Locate every blood parasite and identify its species.
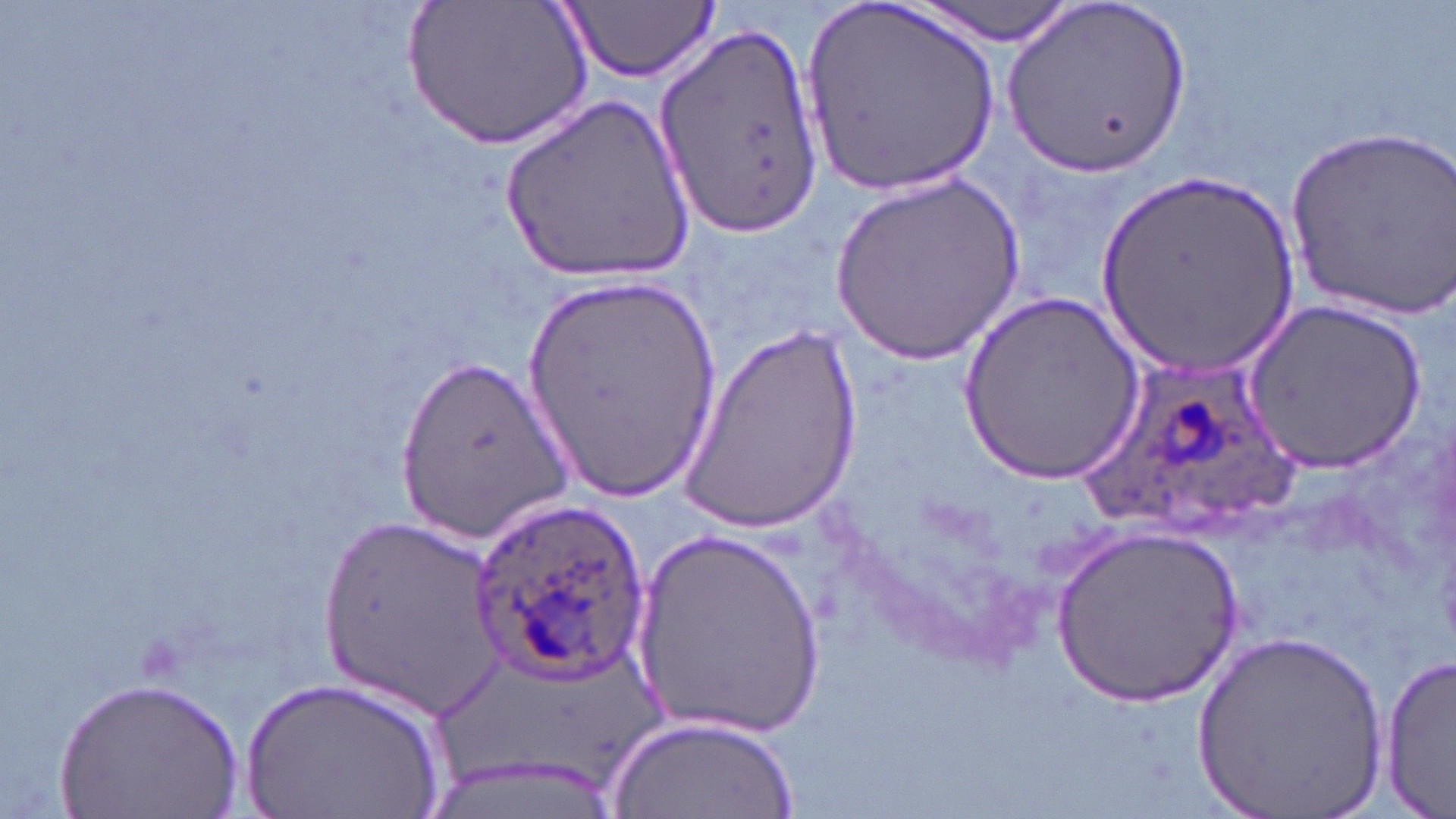

Approximate bounding boxes as [x1, y1, x2, y2] in pixels.
Plasmodium ovale-infected red blood cells: [1080, 354, 1309, 532], [468, 493, 653, 687].
No Plasmodium falciparum, Plasmodium malariae, Plasmodium vivax, Babesia divergens, or Trypanosoma brucei observed.

{
  "slide_level_diagnosis": "Plasmodium ovale",
  "magnification": "1000x",
  "preparation": "thin blood film",
  "image_size": "1456×819 pixels",
  "stain": "May-Grünwald-Giemsa",
  "modality": "light microscopy",
  "field_of_view": "one of a larger specimen",
  "uninfected_red_blood_cell_locations": "approximate bounding boxes as [x1, y1, x2, y2] in pixels: [407, 0, 591, 152], [560, 0, 720, 82], [907, 0, 1082, 43], [1005, 0, 1190, 177], [804, 3, 1000, 200], [658, 25, 822, 238], [502, 94, 697, 284], [1286, 124, 1455, 319], [1093, 172, 1304, 375], [828, 175, 1025, 364], [520, 272, 725, 505], [958, 291, 1144, 488], [1242, 301, 1427, 474], [672, 320, 864, 529], [397, 352, 572, 542], [312, 519, 509, 707], [1053, 525, 1243, 707], [632, 528, 831, 740], [1194, 627, 1390, 819], [1380, 651, 1456, 813], [50, 674, 242, 818], [237, 677, 453, 817], [608, 713, 801, 817]"
}